Name the parasite shown.
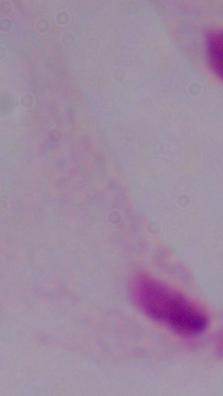

This is a trichomonad.

magnification: 1000x
modality: photomicrograph